State which parasite is depicted.
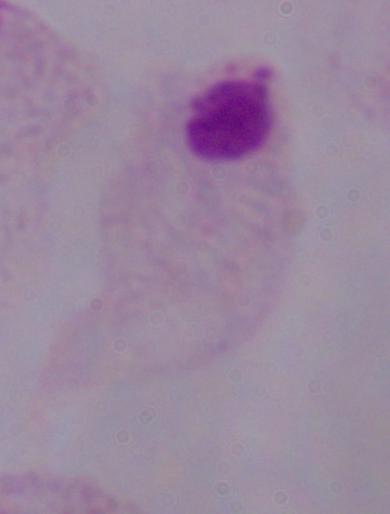

This is a trichomonad.

modality = micrograph
magnification = 1000x